Name the cell type shown.
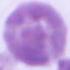

This is an erythrocyte.

Summary:
  - Modality: photomicrograph
  - Magnification: 1000x